Assess this cell for malaria.
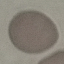
It is uninfected.

Giemsa-stained preparation. Photographed with a smartphone camera at the microscope eyepiece. Thin blood film. Automatically extracted cell patch, resized to 64 × 64 pixels.